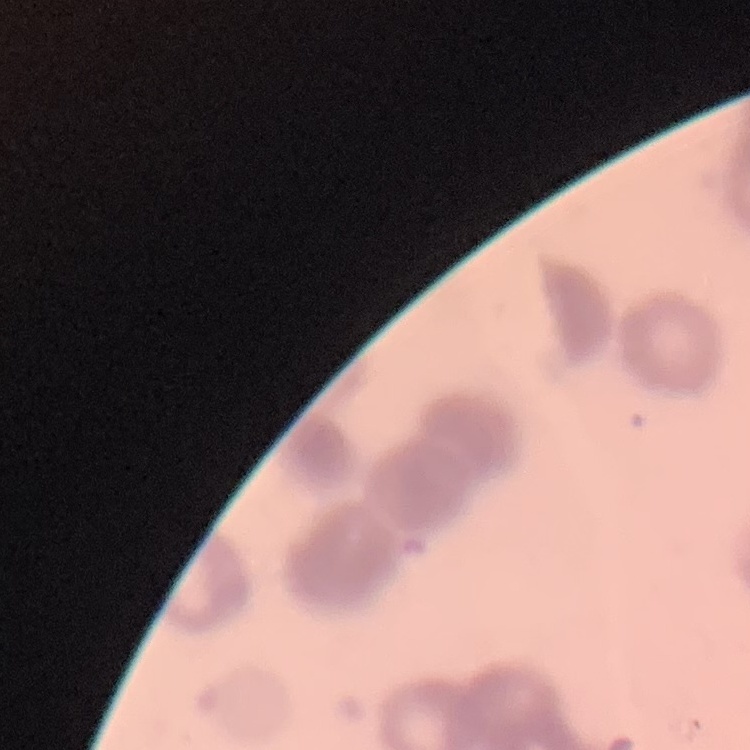
Summary:
  - Erythrocyte morphology: rouleaux formation
  - Stain: Field's or Giemsa
  - Preparation: thin blood smear
  - Image type: square crop of a larger photomicrograph